Outline each blood parasite and name the species.
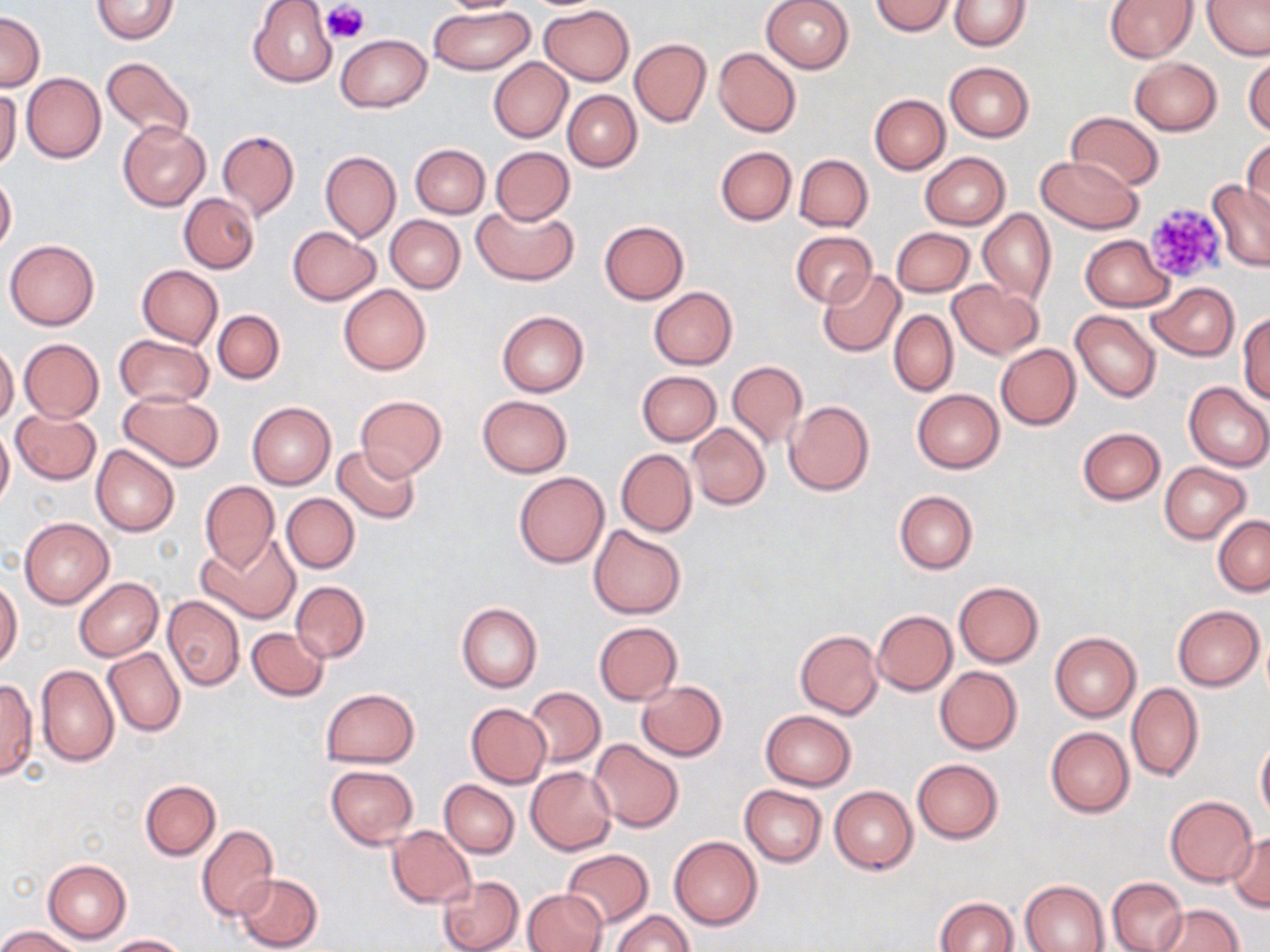
No blood parasites observed.

Approximate bounding boxes as [x1, y1, x2, y2] in pixels. Uninfected red blood cell locations: [91, 0, 179, 44], [248, 0, 338, 87], [434, 0, 532, 15], [759, 0, 854, 74], [948, 0, 1031, 51], [1104, 0, 1196, 62], [1203, 0, 1269, 60], [869, 1, 955, 35], [429, 5, 534, 76], [540, 5, 634, 86], [0, 13, 45, 92], [337, 34, 431, 112], [630, 38, 711, 127], [713, 47, 802, 137], [1244, 53, 1270, 136], [101, 55, 195, 143], [488, 57, 571, 143], [1130, 57, 1221, 135], [944, 61, 1034, 142], [22, 73, 106, 163], [0, 88, 21, 172], [563, 91, 641, 172], [869, 94, 950, 174], [1065, 112, 1165, 191], [117, 120, 210, 211], [217, 130, 299, 221], [1243, 136, 1270, 221], [410, 144, 489, 218], [716, 146, 796, 225], [490, 147, 575, 225], [319, 150, 401, 242], [920, 152, 1010, 229], [794, 154, 872, 232], [1034, 155, 1144, 234], [0, 175, 16, 254], [1207, 181, 1269, 272], [180, 194, 259, 273], [472, 202, 578, 286], [977, 208, 1055, 306], [385, 215, 465, 292], [599, 220, 689, 303], [288, 227, 380, 306], [891, 227, 974, 297], [791, 231, 876, 308], [1081, 235, 1174, 311], [5, 240, 99, 330], [136, 265, 222, 348], [817, 269, 905, 356], [947, 280, 1044, 359], [1148, 282, 1239, 360], [339, 284, 431, 375], [649, 287, 737, 369], [643, 290, 726, 446], [213, 310, 284, 383], [496, 310, 589, 398], [889, 310, 958, 396], [1071, 310, 1161, 402], [1238, 313, 1270, 403], [115, 335, 214, 408], [19, 338, 104, 422], [0, 343, 19, 427], [996, 344, 1081, 429], [726, 361, 807, 449], [636, 370, 720, 446], [1183, 382, 1270, 472], [911, 390, 1004, 474], [118, 391, 224, 471], [477, 395, 573, 477], [354, 396, 447, 481], [784, 400, 874, 496], [248, 401, 335, 490], [11, 410, 102, 484], [687, 422, 770, 511], [0, 427, 14, 508], [1077, 427, 1166, 505], [91, 445, 179, 537], [333, 445, 421, 524], [616, 449, 696, 536], [1159, 462, 1252, 544], [513, 472, 609, 568], [199, 480, 279, 573], [894, 491, 977, 574], [281, 493, 359, 573], [1213, 515, 1270, 597], [20, 517, 113, 608], [589, 524, 686, 619], [198, 534, 301, 624], [0, 576, 22, 671], [74, 577, 163, 661], [291, 581, 370, 662], [953, 581, 1044, 667], [162, 595, 245, 691], [456, 601, 542, 692], [1172, 605, 1264, 690], [872, 610, 957, 695], [594, 622, 682, 704], [247, 627, 329, 702], [795, 630, 882, 719], [1050, 632, 1141, 722], [103, 648, 185, 737], [35, 665, 119, 766], [935, 666, 1023, 754], [0, 677, 37, 781], [635, 681, 727, 760], [1126, 683, 1204, 782], [524, 686, 605, 767], [320, 687, 418, 766], [466, 703, 551, 787], [759, 710, 856, 790], [1045, 726, 1135, 817], [1256, 735, 1270, 825], [589, 739, 684, 833], [911, 758, 1004, 844], [325, 765, 419, 848], [527, 767, 615, 853], [139, 780, 220, 860], [440, 780, 519, 857], [739, 785, 826, 868], [830, 785, 918, 874], [1165, 795, 1256, 886], [197, 825, 279, 921], [387, 826, 475, 908], [1227, 831, 1270, 911], [669, 836, 763, 930], [561, 849, 654, 928], [43, 858, 131, 943], [234, 872, 324, 951], [436, 875, 523, 952], [1106, 876, 1188, 952], [1020, 879, 1110, 952], [521, 889, 608, 952], [933, 897, 1019, 952], [1152, 903, 1244, 951], [611, 910, 692, 952], [0, 926, 81, 952], [105, 933, 190, 951]. Platelet locations: [323, 2, 368, 46], [1141, 201, 1228, 286]. Slide-level diagnosis: no evidence of blood parasites. Thin blood film. Image is 1270×952 pixels. Captured at 1000x magnification. Optical microscopy. May-Grünwald-Giemsa stain. Single field of view.